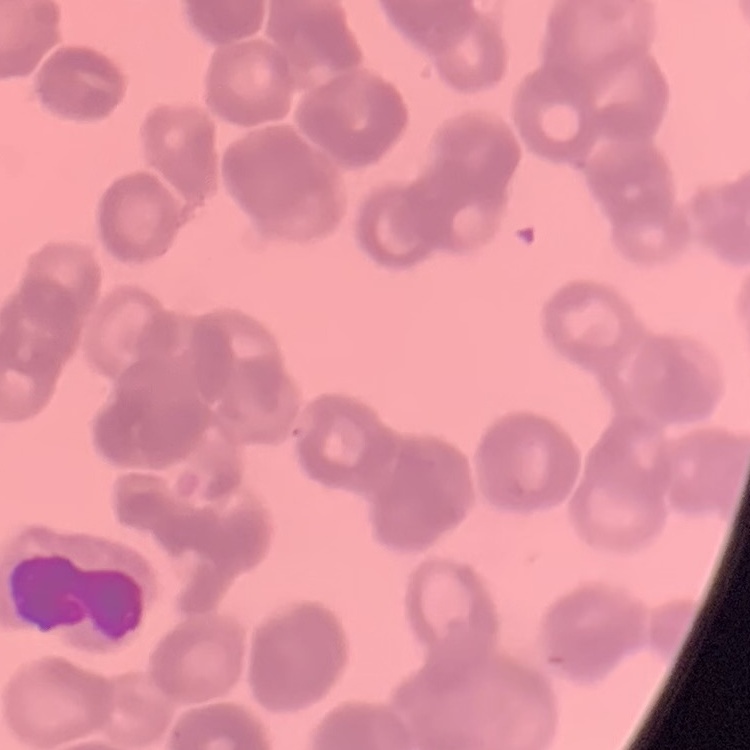 The erythrocytes show rouleaux formation. Thin blood smear. One tile cut from a larger photomicrograph. Field's or Giemsa stain.